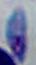

Summary:
  - Magnification: 1000x
  - Identification: Toxoplasma gondii
  - Modality: photomicrograph